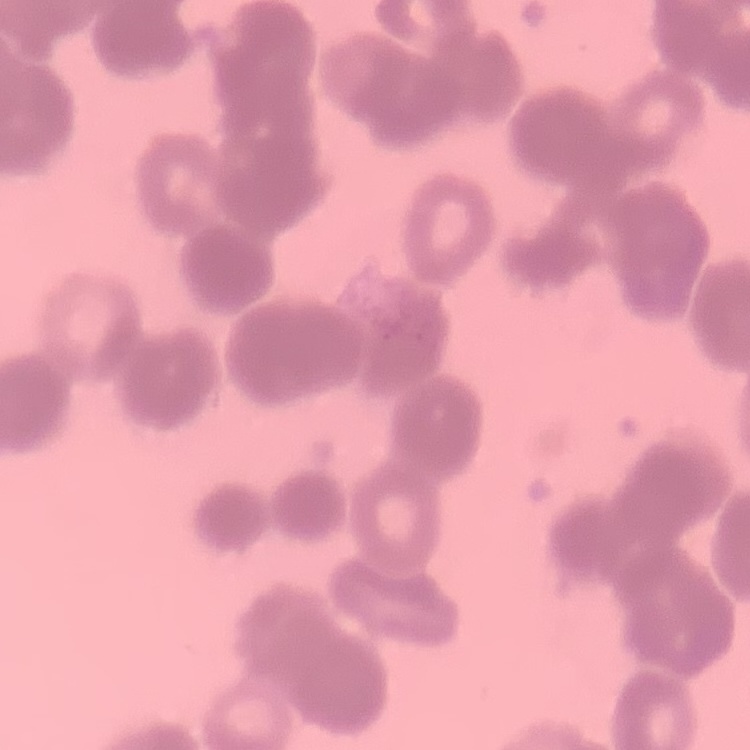

The erythrocytes exhibit rouleaux formation. One tile cut from a larger photomicrograph. Stained with either Field's or Giemsa. Thin peripheral smear.